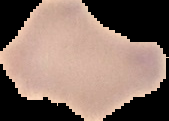
image_type: cell region segmented out of the field of view; surrounding area masked to black
image_size: 169×121 pixels
preparation: thin blood smear
malaria_status: uninfected